Classify this cell by malaria status.
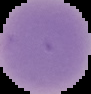
Uninfected.

From a thin blood film. Image is 91×94 pixels. The area outside the segmented cell region is set to black.